Locate every Plasmodium ovale-infected red blood cell.
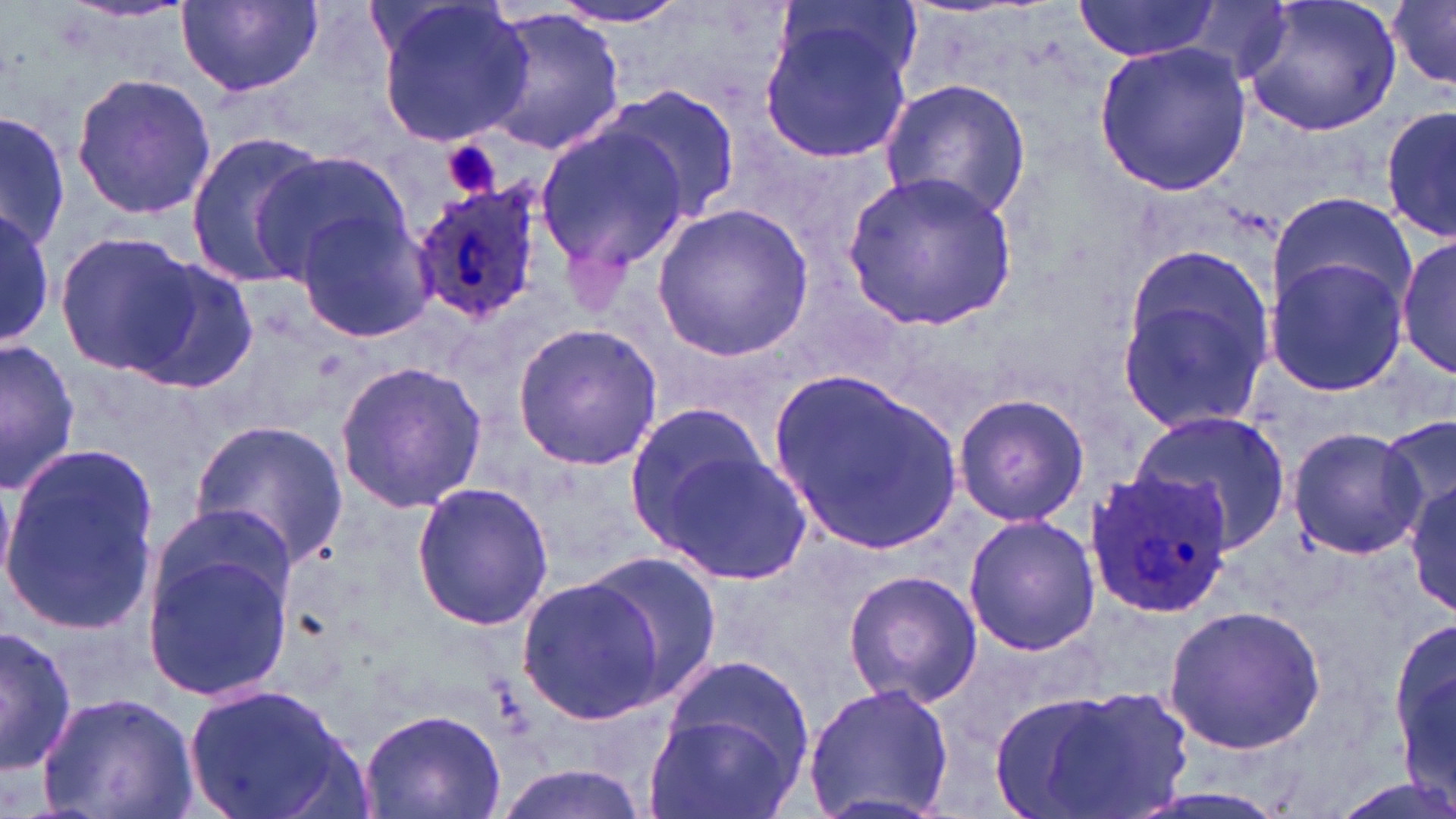

Approximate bounding boxes as named x1/y1/x2/y2 corners in pixels.
Plasmodium ovale-infected red blood cells: (x1=408, y1=182, x2=547, y2=328), (x1=1082, y1=471, x2=1233, y2=621).

Uninfected red blood cell locations: (x1=1237, y1=0, x2=1404, y2=136), (x1=176, y1=1, x2=322, y2=100), (x1=544, y1=1, x2=697, y2=32), (x1=1072, y1=1, x2=1223, y2=62), (x1=371, y1=2, x2=536, y2=145), (x1=1389, y1=2, x2=1455, y2=87), (x1=757, y1=3, x2=920, y2=164), (x1=479, y1=10, x2=626, y2=153), (x1=1094, y1=41, x2=1252, y2=194), (x1=70, y1=72, x2=217, y2=219), (x1=879, y1=77, x2=1033, y2=224), (x1=602, y1=85, x2=742, y2=227), (x1=1383, y1=100, x2=1455, y2=245), (x1=1, y1=108, x2=70, y2=254), (x1=535, y1=123, x2=692, y2=279), (x1=184, y1=132, x2=328, y2=287), (x1=253, y1=150, x2=409, y2=281), (x1=844, y1=171, x2=1020, y2=330), (x1=1267, y1=189, x2=1416, y2=315), (x1=650, y1=203, x2=815, y2=361), (x1=0, y1=209, x2=55, y2=345), (x1=293, y1=209, x2=438, y2=345), (x1=53, y1=229, x2=200, y2=378), (x1=1398, y1=232, x2=1455, y2=382), (x1=1263, y1=256, x2=1411, y2=396), (x1=126, y1=258, x2=261, y2=395), (x1=1115, y1=277, x2=1272, y2=438), (x1=511, y1=322, x2=665, y2=471), (x1=1, y1=339, x2=82, y2=496), (x1=335, y1=361, x2=487, y2=513), (x1=771, y1=371, x2=964, y2=556), (x1=953, y1=391, x2=1089, y2=527), (x1=624, y1=400, x2=775, y2=546), (x1=1129, y1=409, x2=1293, y2=556), (x1=1379, y1=413, x2=1455, y2=529), (x1=187, y1=420, x2=347, y2=569), (x1=1288, y1=427, x2=1422, y2=558), (x1=0, y1=441, x2=162, y2=642), (x1=649, y1=443, x2=814, y2=589), (x1=1407, y1=474, x2=1456, y2=620), (x1=411, y1=481, x2=554, y2=632), (x1=961, y1=514, x2=1101, y2=657), (x1=145, y1=515, x2=300, y2=702), (x1=577, y1=553, x2=721, y2=694), (x1=843, y1=570, x2=984, y2=708), (x1=520, y1=576, x2=666, y2=722), (x1=1161, y1=603, x2=1327, y2=754), (x1=1393, y1=608, x2=1454, y2=811), (x1=0, y1=625, x2=77, y2=776), (x1=662, y1=654, x2=817, y2=780), (x1=802, y1=681, x2=955, y2=819), (x1=1012, y1=682, x2=1194, y2=819), (x1=183, y1=684, x2=364, y2=819), (x1=36, y1=691, x2=197, y2=819), (x1=356, y1=707, x2=505, y2=819), (x1=646, y1=714, x2=792, y2=819), (x1=488, y1=764, x2=653, y2=818), (x1=1326, y1=776, x2=1456, y2=819). Platelet locations: (x1=440, y1=138, x2=502, y2=201). Slide-level diagnosis: Plasmodium ovale. Thin blood film. Light microscopy. Image is 1456×819 pixels. May-Grünwald-Giemsa-stained preparation. 1000x magnification. One field of a larger specimen.